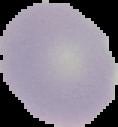

malaria status = uninfected
image type = segmented cell region on a black background
image size = 118×127 pixels
preparation = thin blood film